Name the cell type shown.
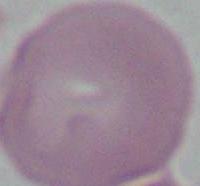
An erythrocyte.

Summary:
  - Modality: micrograph
  - Magnification: 1000x